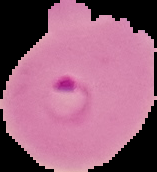
Cell region segmented out of the field of view; the surrounding area is masked to black. From a thin blood film. Malaria status: parasitized. Image is 157×172 pixels.